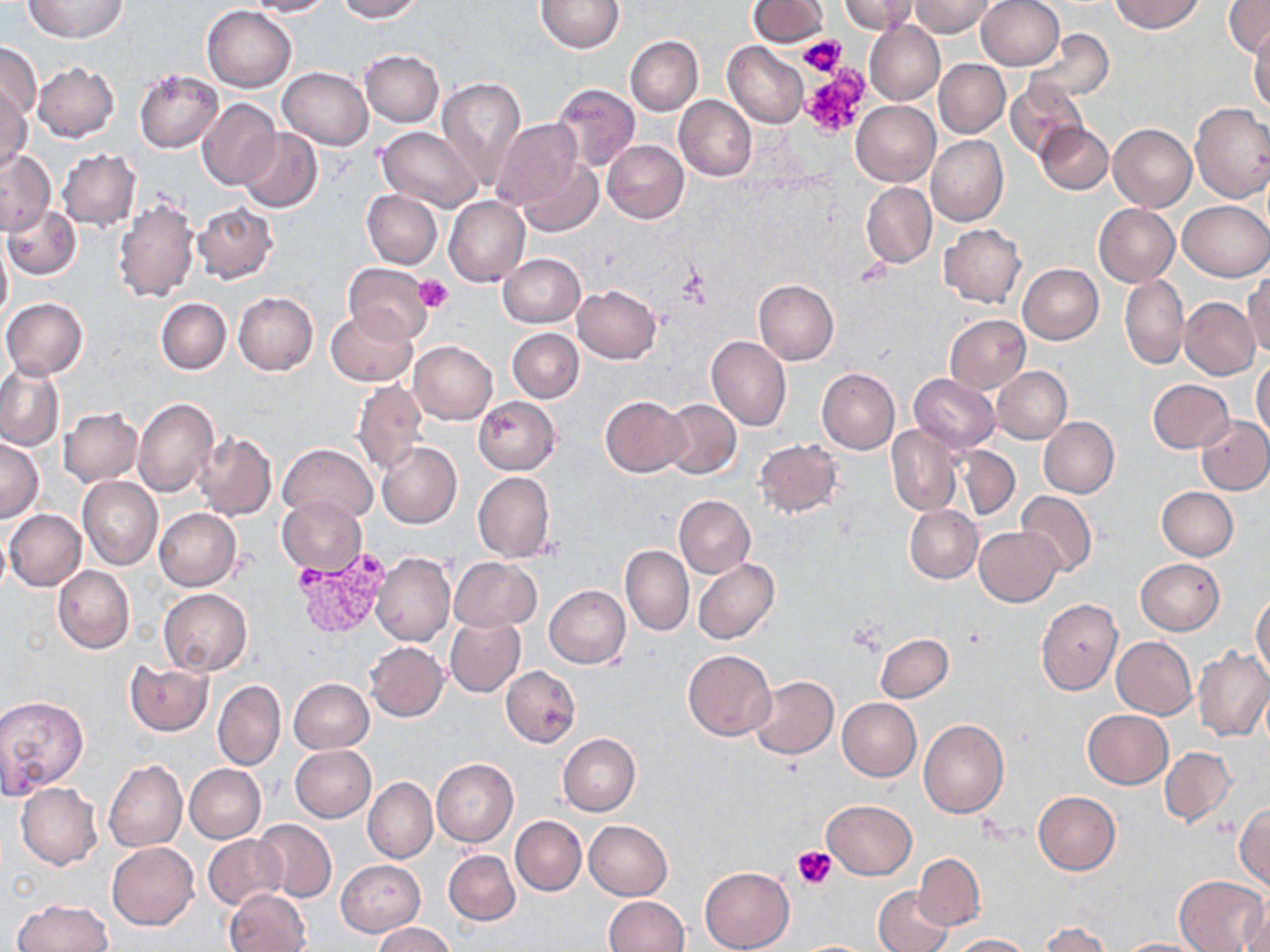 Approximate bounding boxes as (x1, y1, x2, y2) in pixels. Platelet locations: (799, 34, 847, 76), (799, 72, 868, 136), (677, 267, 713, 305), (413, 276, 453, 313), (793, 845, 837, 888). Plasmodium vivax-infected red blood cell locations: (294, 555, 386, 637). Uninfected red blood cell locations: (23, 0, 130, 43), (248, 0, 334, 17), (335, 0, 422, 22), (537, 0, 623, 52), (748, 0, 827, 46), (836, 0, 915, 34), (910, 0, 995, 37), (977, 0, 1064, 71), (1111, 0, 1202, 33), (1224, 1, 1269, 57), (203, 5, 296, 92), (865, 21, 945, 105), (1249, 27, 1270, 113), (1024, 29, 1114, 102), (625, 36, 703, 115), (0, 42, 42, 121), (724, 42, 808, 127), (360, 50, 444, 127), (934, 60, 1009, 137), (32, 63, 119, 141), (278, 66, 372, 149), (133, 68, 223, 153), (436, 76, 526, 191), (1006, 78, 1086, 159), (552, 84, 641, 172), (0, 88, 32, 174), (675, 96, 757, 181), (197, 99, 280, 189), (852, 100, 940, 185), (1190, 101, 1270, 203), (492, 118, 586, 215), (1036, 122, 1113, 194), (1108, 123, 1197, 212), (378, 126, 484, 212), (239, 127, 323, 213), (926, 135, 1008, 226), (934, 138, 1014, 309), (603, 140, 689, 223), (0, 149, 55, 236), (57, 149, 141, 232), (513, 156, 601, 234), (861, 182, 936, 269), (362, 189, 442, 269), (113, 195, 199, 305), (444, 196, 530, 287), (1179, 200, 1269, 280), (193, 201, 277, 284), (1093, 204, 1180, 286), (3, 205, 81, 279), (939, 224, 1025, 308), (0, 240, 12, 327), (499, 253, 586, 327), (343, 263, 434, 343), (1018, 264, 1103, 344), (1244, 272, 1270, 358), (1120, 274, 1189, 369), (754, 279, 839, 365), (572, 285, 660, 363), (233, 291, 318, 375), (1, 297, 88, 380), (1180, 297, 1260, 380), (157, 299, 231, 374), (325, 309, 416, 385), (945, 314, 1031, 393), (508, 328, 584, 403), (707, 335, 790, 432), (409, 341, 497, 424), (1251, 359, 1270, 439), (0, 361, 66, 451), (817, 367, 901, 454), (992, 367, 1071, 445), (908, 373, 1000, 453), (351, 379, 429, 475), (1148, 379, 1234, 453), (473, 396, 560, 474), (600, 396, 690, 477), (134, 397, 217, 497), (661, 400, 741, 480), (60, 408, 143, 486), (1196, 415, 1270, 495), (1039, 417, 1119, 498), (886, 425, 962, 516), (193, 431, 277, 520), (1, 437, 44, 525), (755, 439, 844, 518), (376, 442, 462, 529), (280, 443, 377, 523), (954, 444, 1018, 521), (472, 472, 555, 562), (78, 477, 162, 572), (1156, 487, 1237, 561), (1016, 490, 1097, 576), (674, 495, 756, 579), (277, 496, 365, 577), (905, 505, 982, 582), (154, 508, 241, 591), (4, 510, 86, 591), (0, 523, 10, 598), (974, 526, 1065, 608), (621, 546, 694, 637), (371, 552, 455, 647), (450, 556, 541, 632), (693, 557, 779, 645), (1135, 557, 1225, 635), (53, 565, 134, 653), (544, 585, 631, 669), (157, 588, 252, 675), (1251, 595, 1270, 679), (1035, 598, 1123, 695), (444, 617, 526, 697), (875, 633, 953, 702), (1111, 636, 1196, 719), (365, 641, 449, 722), (1193, 648, 1269, 742), (682, 650, 776, 740), (124, 660, 212, 735), (500, 665, 581, 747), (748, 677, 837, 758), (288, 678, 374, 753), (212, 679, 285, 771), (216, 683, 369, 762), (0, 695, 89, 797), (836, 698, 921, 781), (1083, 710, 1173, 789), (919, 719, 1008, 817), (558, 733, 640, 816), (289, 745, 376, 823), (1160, 747, 1236, 827), (431, 758, 518, 847), (104, 759, 187, 852), (185, 764, 266, 843), (363, 777, 438, 863), (16, 783, 103, 869), (1032, 792, 1120, 874), (823, 799, 917, 879), (1233, 801, 1270, 889), (511, 815, 587, 895), (253, 820, 337, 902), (584, 820, 673, 901), (202, 834, 286, 910), (107, 841, 199, 929), (444, 850, 519, 925), (912, 853, 985, 931), (336, 859, 426, 937), (699, 866, 795, 951), (1173, 875, 1268, 952), (872, 887, 953, 952), (226, 888, 311, 952), (1241, 891, 1269, 952), (603, 895, 688, 952), (10, 899, 111, 952), (1039, 922, 1113, 952), (371, 924, 454, 952), (949, 933, 1034, 951), (1115, 939, 1210, 951). Slide-level diagnosis: Plasmodium vivax. Thin blood smear. May-Grünwald-Giemsa stain. Light microscopy. Single field of view. Image is 1270×952 pixels. Captured at 1000x magnification.